Assess this cell for malaria.
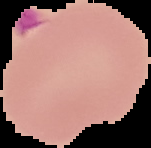
It is parasitized.

Summary:
  - Image type: segmented cell region with the area outside set to black
  - Image size: 151×148 pixels
  - Preparation: thin blood smear